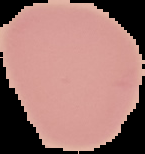
preparation = thin blood smear
image type = segmented cell region with the area outside set to black
result = negative for Plasmodium parasites
image size = 145×154 pixels